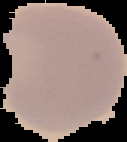
malaria status = uninfected
image size = 127×142 pixels
preparation = thin blood smear
image type = cell region segmented out of the field of view; surrounding area masked to black